Assess for malaria.
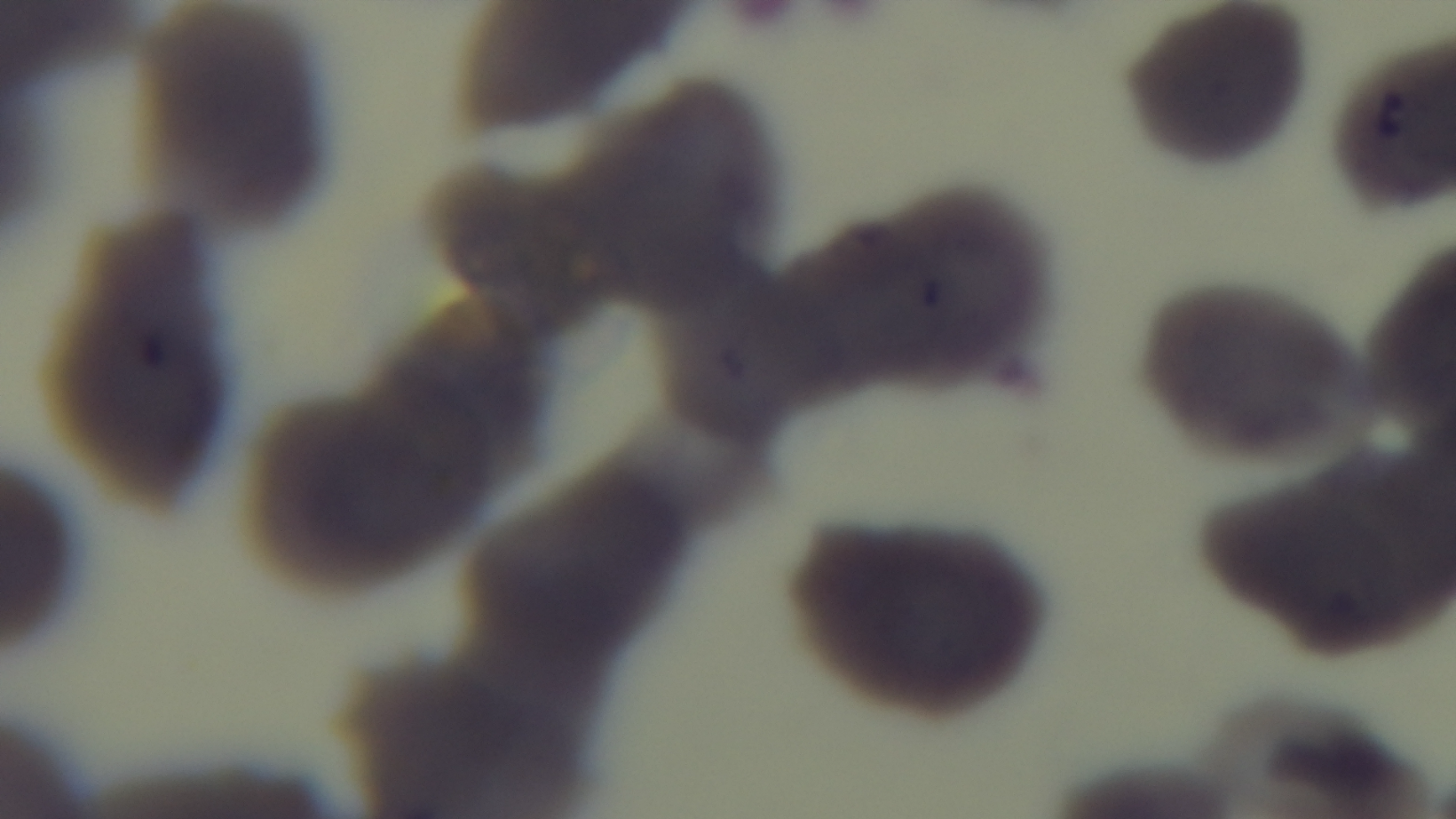
It is uninfected.

Summary:
  - Preparation: thin smear
  - Field of view: single
  - Modality: light microscopy
  - Stain: Giemsa
  - Objective: 100x oil immersion
  - Capture: mounted 4K digital camera